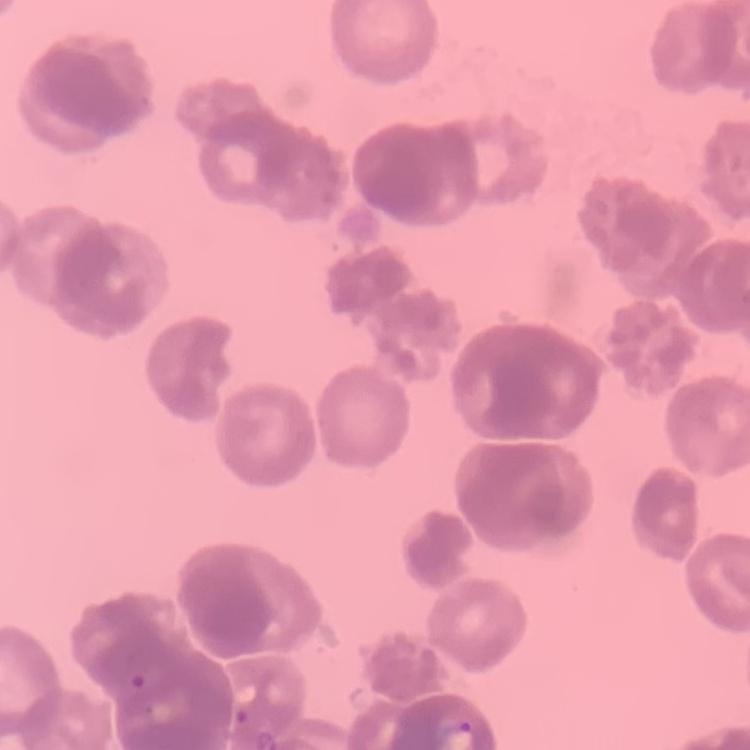
Summary:
  - Red blood cell morphology: rouleaux formation
  - Preparation: thin peripheral smear
  - Stain: Field's or Giemsa
  - Image type: square crop of a larger photomicrograph